Classify this cell by malaria status.
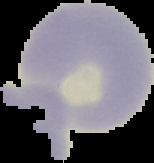

Uninfected.

Summary:
  - Image type: cell region segmented out of the field of view; surrounding area masked to black
  - Preparation: thin blood smear
  - Image size: 154×163 pixels